Assess this cell for malaria.
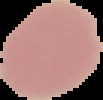
It is uninfected.

preparation = thin blood film
image size = 103×100 pixels
image type = segmented cell region with the area outside set to black